Identify the cell.
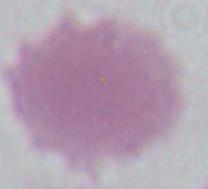
This is an erythrocyte.

Photomicrograph. Captured at 1000x magnification.